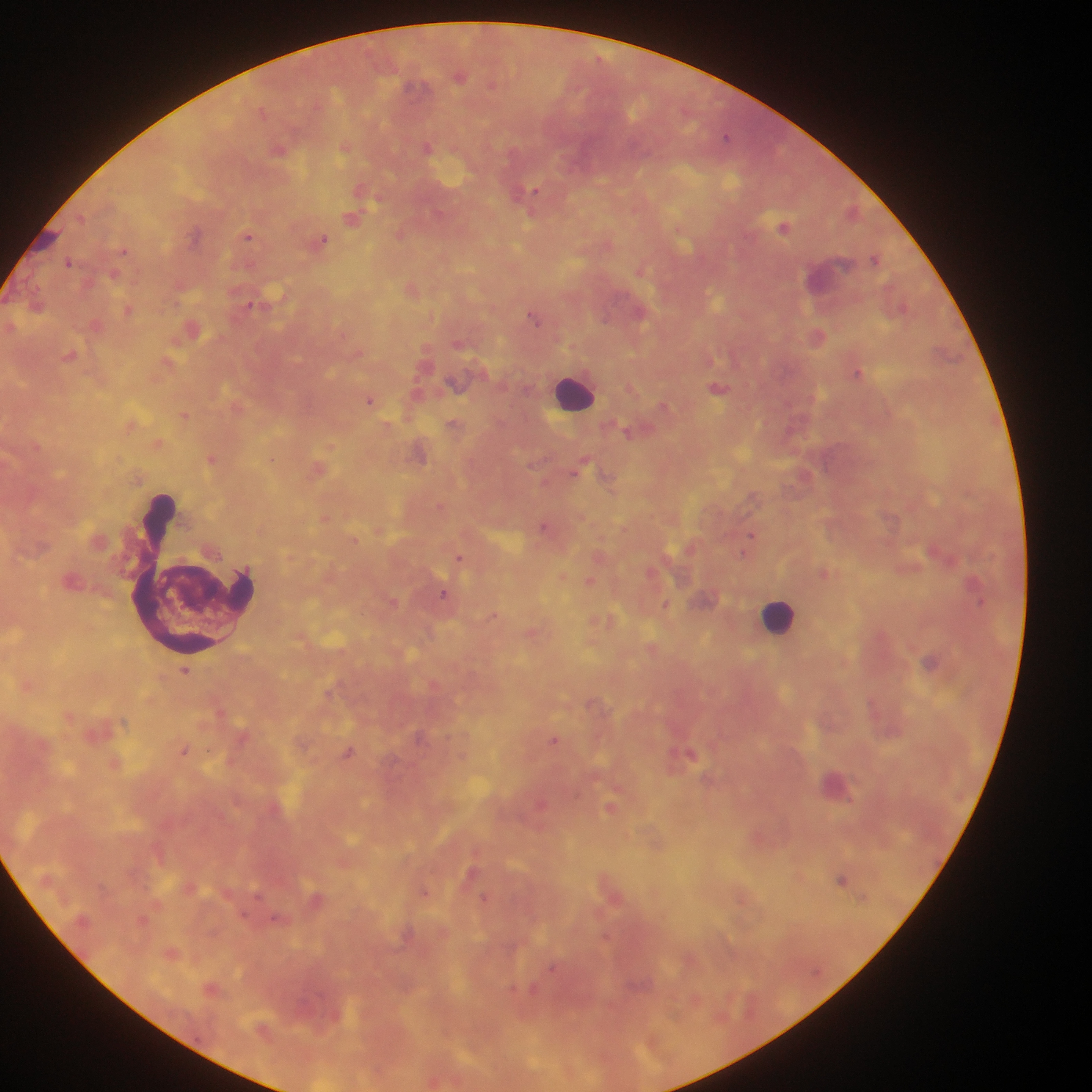
image_size: 1092×1092 pixels
capture: mobile-phone photograph through a microscope
preparation: thick blood smear
country: Ghana
plasmodium_parasite_locations: 'approximate centers as x y in pixels: 459 76; 411 86; 726 136; 427 148; 278 149; 534 191; 352 218; 784 226; 195 234; 400 234; 247 236; 323 239; 123 250; 875 258; 68 262; 128 310; 534 317; 817 337; 858 372; 718 388; 369 400; 663 405; 184 415; 626 431; 211 459; 273 460; 580 468; 752 497; 544 525; 750 537; 355 541; 746 548; 933 552; 458 558; 590 581; 443 593; 979 602; 666 605; 930 662; 185 671; 553 739; 183 750; 348 753; 690 753; 610 808; 840 879; 424 892; 484 897; 552 968'
leukocyte_locations: 'approximate centers as x y in pixels: 573 392; 192 572; 779 616'
field_of_view: single